Report the malaria status of this cell.
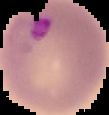

Parasitized.

image_size: 109×115 pixels
image_type: segmented cell region on a black background
preparation: thin blood film